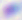

Summary:
  - Modality: photomicrograph
  - Identification: Toxoplasma gondii
  - Magnification: 400x